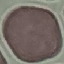
Summary:
  - Malaria status: uninfected
  - Preparation: thin blood film
  - Capture: smartphone camera at the microscope eyepiece
  - Image type: automatically extracted cell patch, resized to 64 × 64 pixels
  - Stain: Giemsa